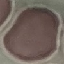

Summary:
  - Result: negative for malaria parasites
  - Capture: smartphone camera at the microscope eyepiece
  - Stain: Giemsa
  - Preparation: thin blood smear
  - Image type: cell patch, automatically extracted from a larger field of view and resized to 64 × 64 pixels